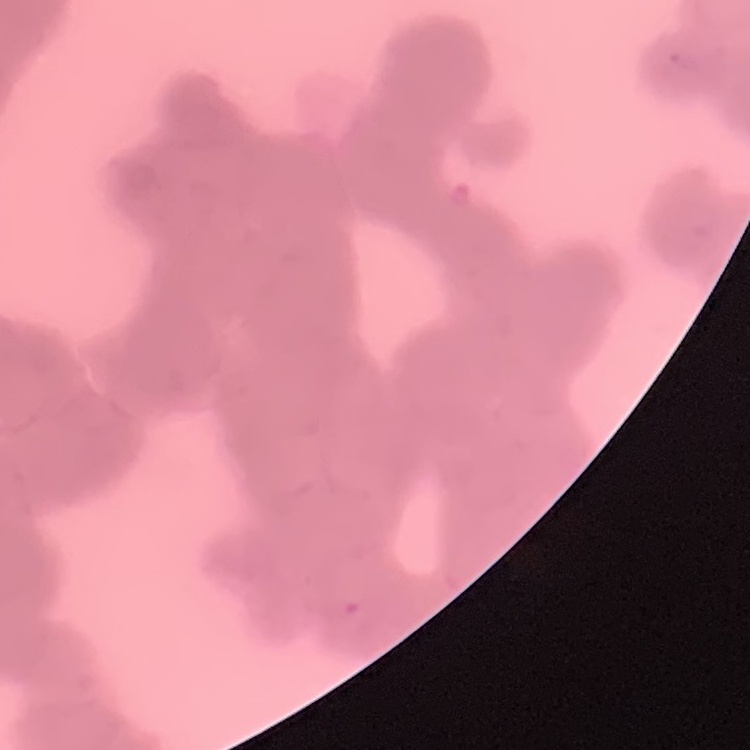

erythrocyte_morphology: rouleaux formation
stain: Field's or Giemsa
preparation: thin peripheral smear
image_type: one tile cut from a larger photomicrograph